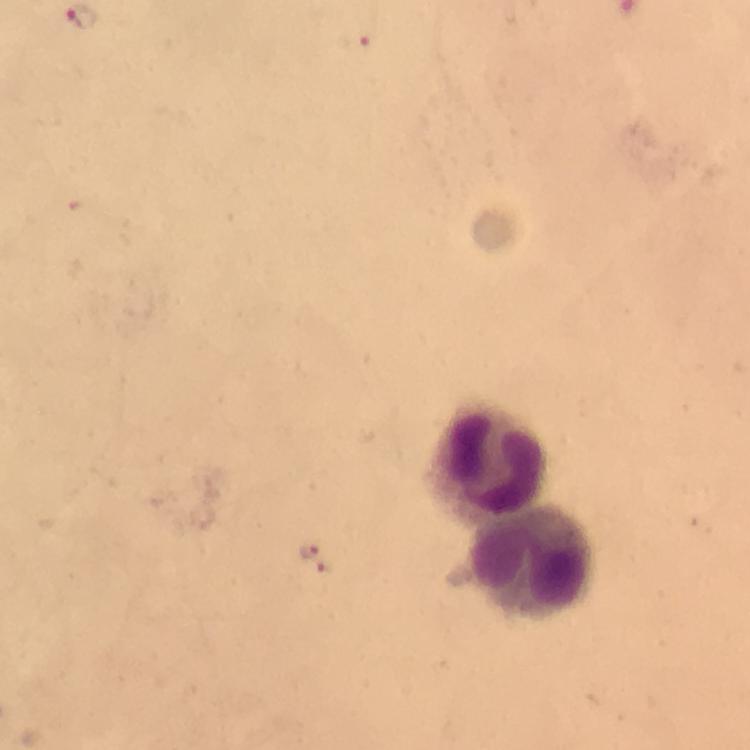
leukocyte_locations: 'approximate centers as {x, y} in pixels: {489, 457}, {533, 563}'
image_size: 750×750 pixels
immersion_oil: applied
magnification: 100x
preparation: thick blood smear
malaria_parasite_locations: 'approximate centers as {x, y} in pixels: {357, 41}, {308, 550}, {326, 567}'
cropped_from: a single field of view
context: from a diagnostic examination for malaria
stain: Giemsa
capture: smartphone mounted on the microscope